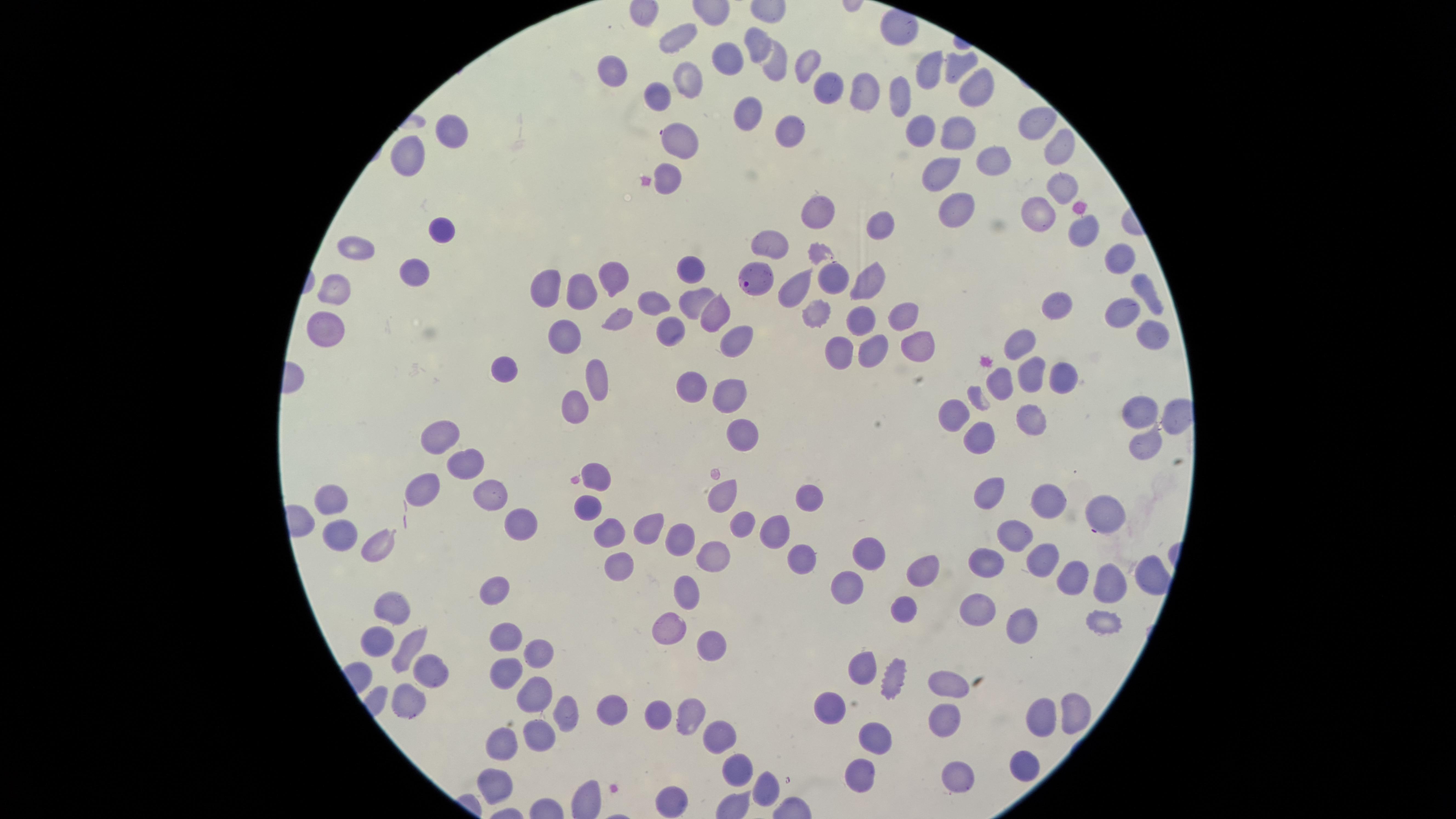
stain: Giemsa
uninfected_red_blood_cells: 'approximate marker points, in pixels from the top-left corner: (x=680, y=34), (x=758, y=41), (x=725, y=62), (x=800, y=65), (x=774, y=68), (x=959, y=68), (x=619, y=70), (x=930, y=78), (x=686, y=86), (x=830, y=91), (x=657, y=92), (x=976, y=95), (x=863, y=96), (x=902, y=102), (x=1032, y=119), (x=749, y=120), (x=916, y=131), (x=455, y=132), (x=791, y=134), (x=960, y=136), (x=681, y=139), (x=1057, y=149), (x=406, y=154), (x=988, y=159), (x=938, y=168), (x=669, y=175), (x=1059, y=185), (x=961, y=208), (x=1038, y=211), (x=819, y=214), (x=879, y=222), (x=1080, y=227), (x=444, y=231), (x=777, y=245), (x=357, y=253), (x=1114, y=263), (x=691, y=272), (x=418, y=276), (x=831, y=278), (x=549, y=280), (x=614, y=280), (x=866, y=284), (x=586, y=285), (x=794, y=286), (x=335, y=287), (x=1146, y=294), (x=691, y=297), (x=654, y=304), (x=1055, y=305), (x=817, y=307), (x=1123, y=314), (x=623, y=316), (x=896, y=316), (x=855, y=317), (x=709, y=318), (x=332, y=328), (x=564, y=328), (x=1150, y=338), (x=736, y=342), (x=912, y=346), (x=865, y=347), (x=1024, y=347), (x=836, y=360), (x=503, y=368), (x=1026, y=375), (x=596, y=377), (x=1057, y=378), (x=997, y=383), (x=697, y=384), (x=734, y=400), (x=1138, y=410), (x=576, y=414), (x=1034, y=415), (x=949, y=417), (x=437, y=437), (x=746, y=438), (x=981, y=439), (x=1140, y=446), (x=465, y=462), (x=601, y=479), (x=425, y=486), (x=491, y=492), (x=990, y=492), (x=1049, y=494), (x=723, y=496), (x=810, y=497), (x=334, y=499), (x=591, y=508), (x=1111, y=515), (x=744, y=524), (x=515, y=530), (x=650, y=530), (x=776, y=531), (x=614, y=534), (x=679, y=536), (x=344, y=539), (x=380, y=540), (x=1015, y=541), (x=714, y=557), (x=803, y=557), (x=870, y=557), (x=620, y=558), (x=1050, y=559), (x=984, y=562), (x=918, y=575), (x=1071, y=575), (x=1148, y=579), (x=1107, y=586), (x=497, y=588), (x=845, y=594), (x=689, y=600), (x=390, y=608), (x=908, y=608), (x=974, y=611), (x=1105, y=624), (x=1018, y=629), (x=671, y=631), (x=503, y=637), (x=376, y=638), (x=406, y=646), (x=715, y=654), (x=536, y=656), (x=859, y=669), (x=434, y=672), (x=501, y=676), (x=891, y=676), (x=947, y=684), (x=412, y=695), (x=531, y=695), (x=830, y=711), (x=1080, y=712), (x=611, y=713), (x=688, y=713), (x=654, y=714), (x=566, y=715), (x=1039, y=716), (x=944, y=719), (x=540, y=738), (x=871, y=740), (x=721, y=742), (x=505, y=743), (x=1018, y=770), (x=740, y=772), (x=853, y=776), (x=953, y=778), (x=497, y=780), (x=771, y=790), (x=674, y=799)'
parasitized_red_blood_cells: 'approximate marker points, in pixels from the top-left corner: (x=747, y=277)'
presence: malaria parasites seen
image_size: 1456×819 pixels
visible_region: circular
species: Plasmodium falciparum
preparation: thin blood smear
capture: smartphone photograph through the microscope eyepiece
field_of_view: single